Comment on the morphology of the erythrocytes.
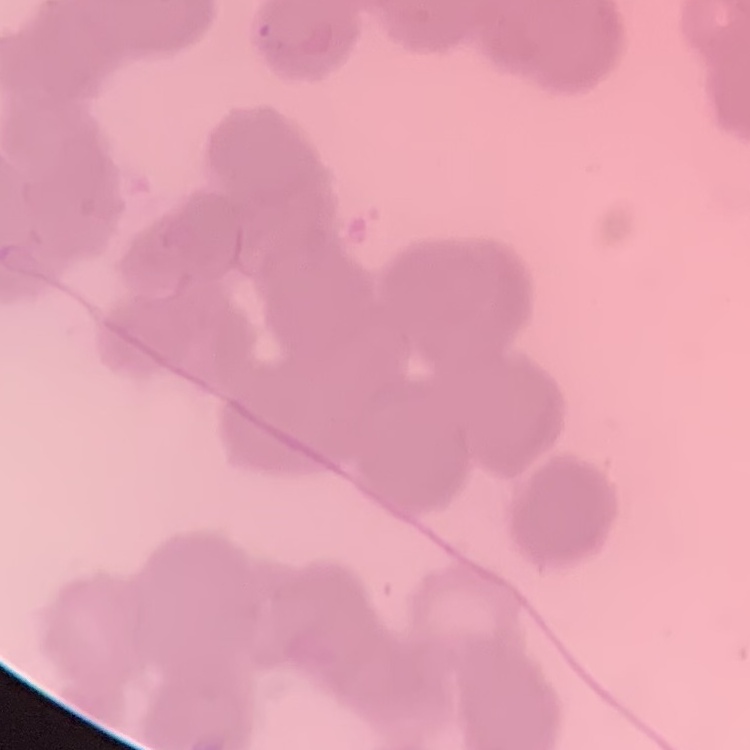

Rouleaux formation.

Square crop of a larger photomicrograph. Thin peripheral smear. Stained with either Field's or Giemsa.